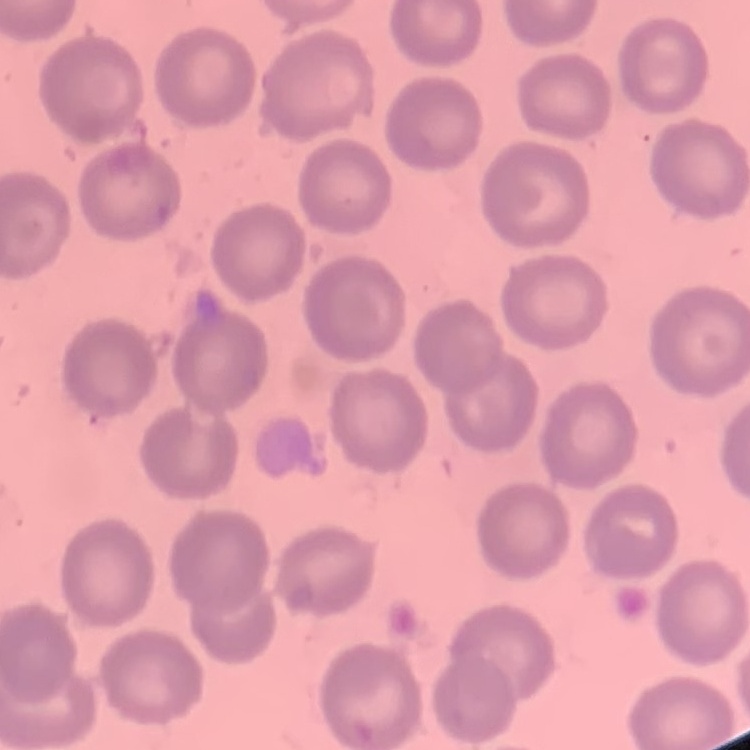

red blood cell morphology = no rouleaux formation
stain = Field's or Giemsa
preparation = thin blood film
image type = one tile cut from a larger photomicrograph